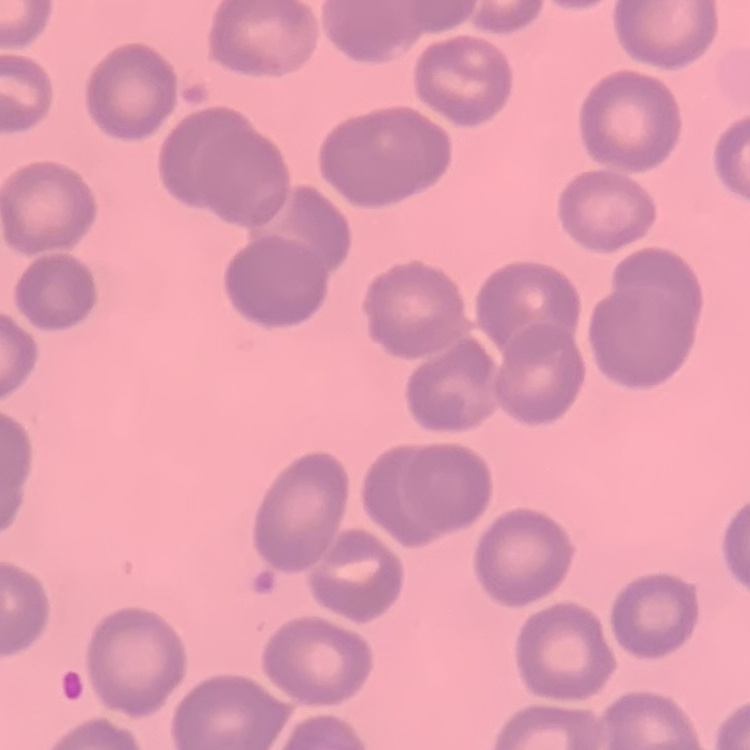

erythrocyte morphology = no rouleaux formation
image type = square crop of a larger photomicrograph
stain = Field's or Giemsa
preparation = thin blood film